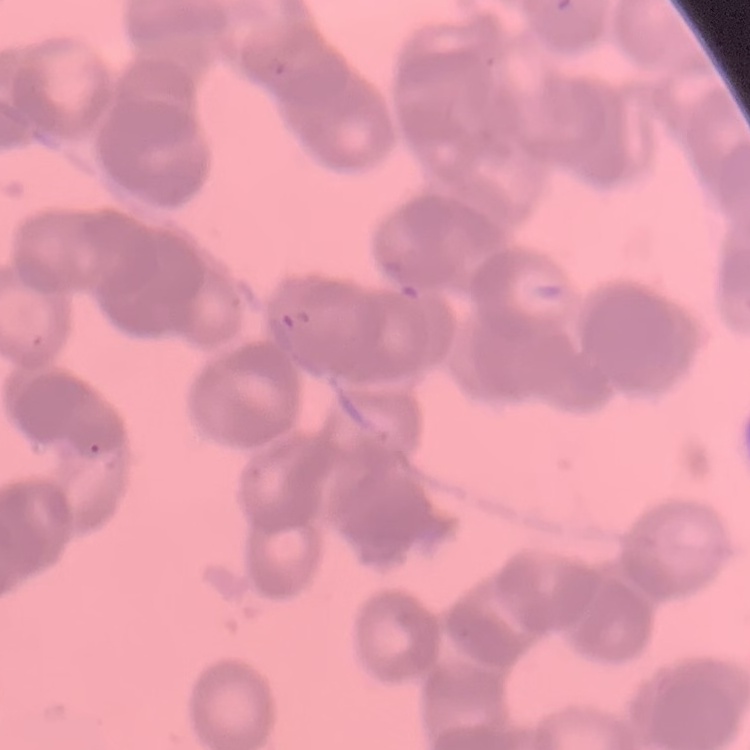

The erythrocytes exhibit rouleaux formation. Stained with either Field's or Giemsa. One tile cut from a larger photomicrograph. Thin peripheral smear.